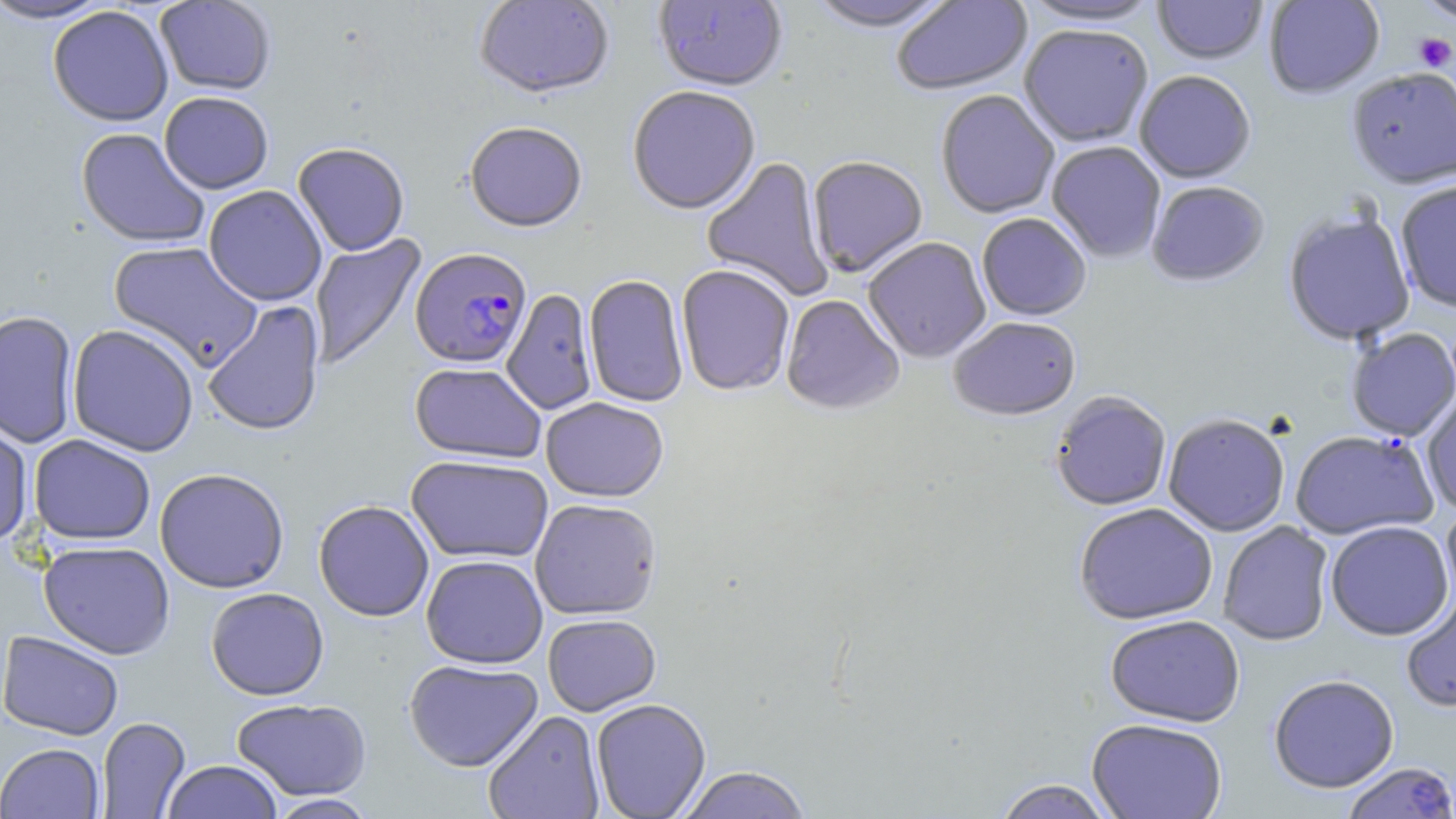 Approximate bounding boxes as [x1, y1, x2, y2] in pixels. Uninfected red blood cell locations: [0, 0, 113, 24], [474, 0, 615, 102], [652, 0, 788, 93], [891, 0, 1033, 97], [1017, 0, 1167, 30], [1153, 0, 1267, 66], [1264, 0, 1384, 100], [1415, 0, 1456, 26], [154, 1, 276, 96], [804, 1, 958, 35], [47, 5, 174, 126], [1018, 26, 1154, 149], [1346, 70, 1456, 191], [1135, 72, 1256, 185], [628, 87, 761, 217], [159, 91, 274, 194], [936, 91, 1059, 220], [464, 124, 588, 234], [75, 127, 210, 248], [1046, 142, 1166, 263], [293, 143, 410, 256], [701, 157, 833, 301], [808, 158, 928, 278], [1395, 181, 1456, 314], [1146, 182, 1270, 289], [204, 185, 327, 306], [1283, 210, 1416, 347], [976, 215, 1091, 322], [309, 234, 427, 371], [863, 238, 991, 364], [108, 241, 263, 372], [677, 266, 795, 397], [583, 276, 689, 408], [502, 288, 598, 415], [780, 295, 904, 417], [202, 300, 326, 438], [0, 309, 79, 449], [948, 318, 1082, 423], [67, 324, 199, 457], [1345, 328, 1456, 441], [410, 362, 546, 465], [1420, 391, 1456, 516], [1050, 392, 1171, 512], [541, 398, 669, 503], [0, 414, 34, 549], [1163, 415, 1290, 537], [1292, 430, 1437, 545], [28, 434, 156, 545], [406, 455, 554, 565], [154, 467, 290, 593], [530, 499, 662, 621], [313, 500, 434, 622], [1074, 504, 1218, 626], [1440, 506, 1456, 613], [1325, 521, 1454, 641], [1218, 522, 1334, 647], [38, 541, 175, 659], [421, 555, 548, 669], [205, 587, 329, 701], [1401, 592, 1456, 714], [542, 615, 661, 716], [1105, 615, 1245, 727], [0, 631, 124, 740], [404, 659, 543, 773], [1268, 675, 1400, 794], [231, 698, 372, 801], [591, 699, 711, 819], [483, 710, 605, 819], [96, 717, 190, 818], [1086, 719, 1228, 819], [1, 742, 105, 818], [161, 760, 284, 819], [1340, 761, 1456, 818], [678, 767, 812, 818], [993, 779, 1116, 819], [266, 794, 379, 818]. Platelet locations: [1412, 33, 1455, 72]. Plasmodium falciparum-infected red blood cell locations: [410, 248, 532, 369]. Slide-level diagnosis: Plasmodium falciparum. Image is 1456×819 pixels. Thin blood film. Captured at 1000x magnification. Light microscopy. May-Grünwald-Giemsa stain. Single field of view.